Point out each leukocyte.
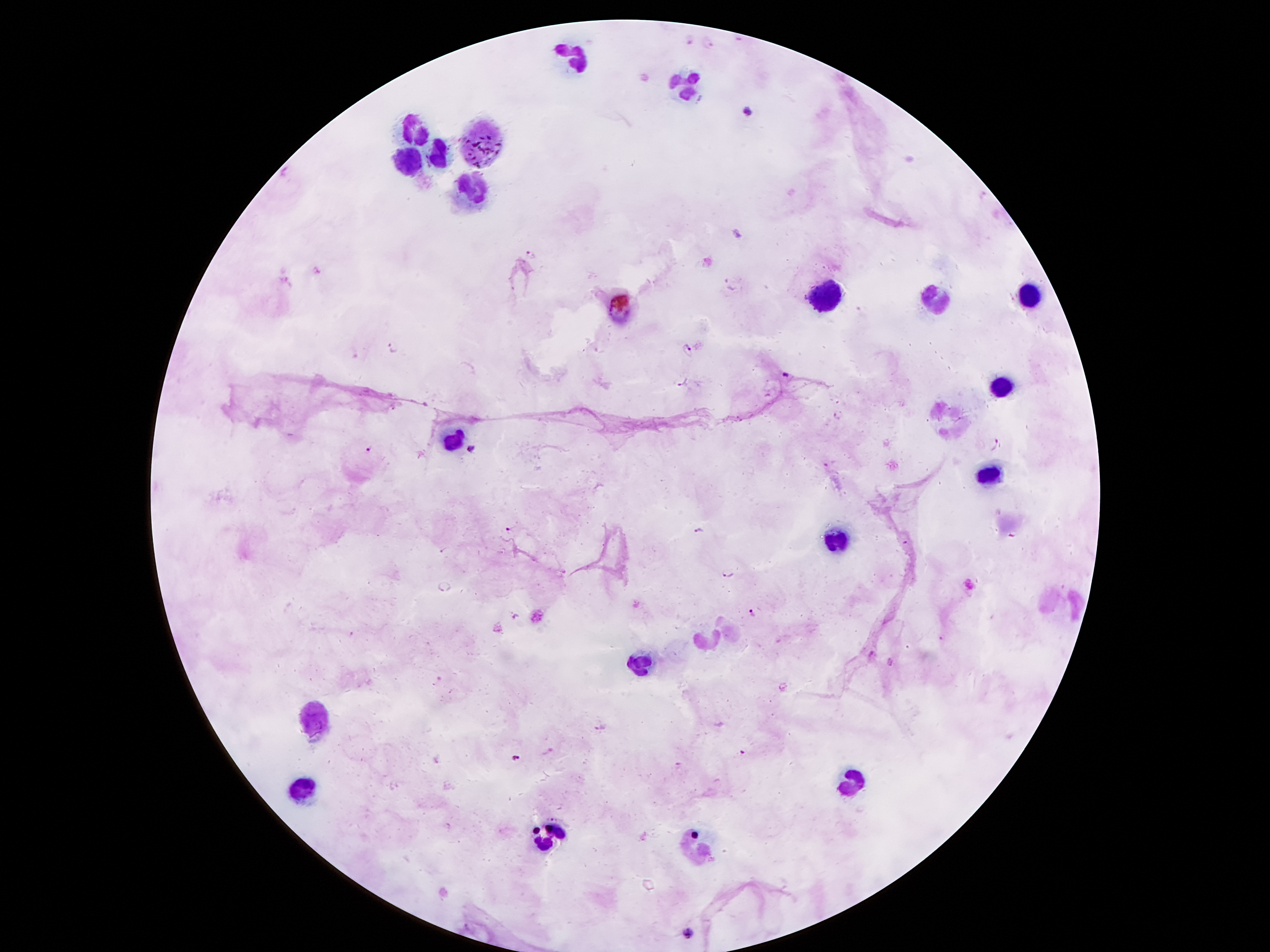
Approximate centers as [x, y] in pixels.
Leukocytes: [577, 55], [682, 86], [416, 132], [483, 141], [441, 155], [409, 162], [472, 187], [825, 296], [932, 296], [1029, 296], [1002, 386], [951, 420], [454, 437], [991, 472], [836, 539], [706, 640], [640, 663], [311, 718], [848, 783], [307, 787], [552, 837], [699, 848].

Plasmodium parasite locations: [738, 39], [691, 40], [709, 44], [746, 112], [740, 234], [530, 255], [393, 345], [688, 351], [784, 374], [681, 381], [837, 416], [997, 445], [368, 450], [471, 450], [825, 465], [508, 529], [700, 531], [444, 549], [728, 573], [445, 586], [752, 612], [516, 617], [352, 634], [942, 637], [872, 652], [891, 661], [600, 728], [516, 758], [553, 818], [689, 933]. Patient malaria status: positive for Plasmodium falciparum. Image is 1270×952 pixels. Single field of view. Giemsa-stained preparation. Smartphone photograph taken through the microscope eyepiece. 100x magnification. Thick blood smear.